State which parasite is depicted.
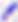
This is Toxoplasma gondii.

Summary:
  - Modality: photomicrograph
  - Magnification: 400x